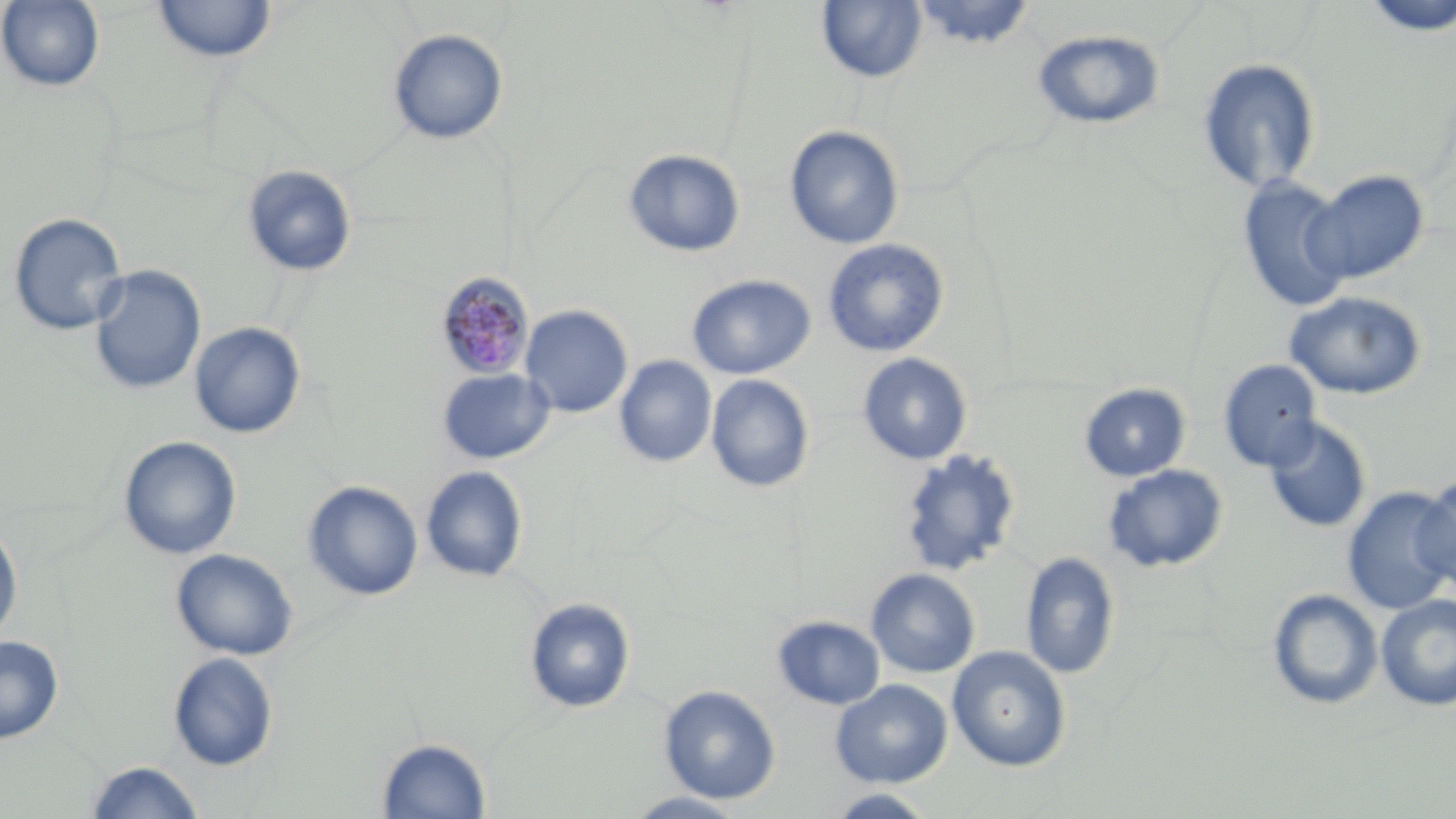

Summary:
  - Coordinate format: approximate bounding boxes as (x1, y1, x2, y2) in pixels
  - Uninfected red blood cell locations: (0, 0, 106, 93), (1360, 0, 1456, 38), (153, 1, 277, 63), (817, 1, 927, 83), (911, 1, 1036, 50), (388, 28, 508, 145), (1032, 28, 1165, 130), (1197, 57, 1322, 194), (784, 125, 904, 250), (623, 149, 745, 257), (242, 165, 358, 277), (1304, 170, 1429, 285), (1237, 176, 1354, 312), (8, 212, 128, 337), (822, 238, 949, 357), (88, 264, 206, 396), (687, 274, 815, 379), (1283, 291, 1428, 400), (519, 305, 633, 417), (189, 321, 307, 438), (857, 353, 973, 465), (614, 355, 716, 467), (1218, 359, 1323, 471), (437, 368, 555, 464), (706, 374, 815, 493), (1078, 382, 1191, 482), (1262, 417, 1372, 534), (118, 436, 241, 560), (900, 449, 1022, 576), (1101, 464, 1228, 572), (421, 466, 529, 582), (1415, 475, 1456, 594), (302, 480, 423, 600), (1342, 486, 1456, 616), (0, 521, 23, 643), (171, 549, 298, 660), (1020, 551, 1120, 680), (866, 568, 981, 678), (1266, 588, 1383, 711), (1376, 593, 1456, 711), (523, 597, 636, 713), (772, 615, 885, 710), (0, 635, 64, 744), (946, 645, 1072, 771), (168, 652, 279, 771), (830, 679, 952, 788), (658, 684, 781, 804), (377, 737, 492, 818), (83, 760, 206, 819), (825, 788, 940, 818), (624, 790, 751, 818)
  - Plasmodium malariae-infected red blood cell locations: (434, 272, 535, 381)
  - Slide-level diagnosis: Plasmodium malariae
  - Preparation: thin blood smear
  - Field of view: one of a larger specimen
  - Modality: light microscopy
  - Image size: 1456×819 pixels
  - Stain: May-Grünwald-Giemsa
  - Magnification: 1000x